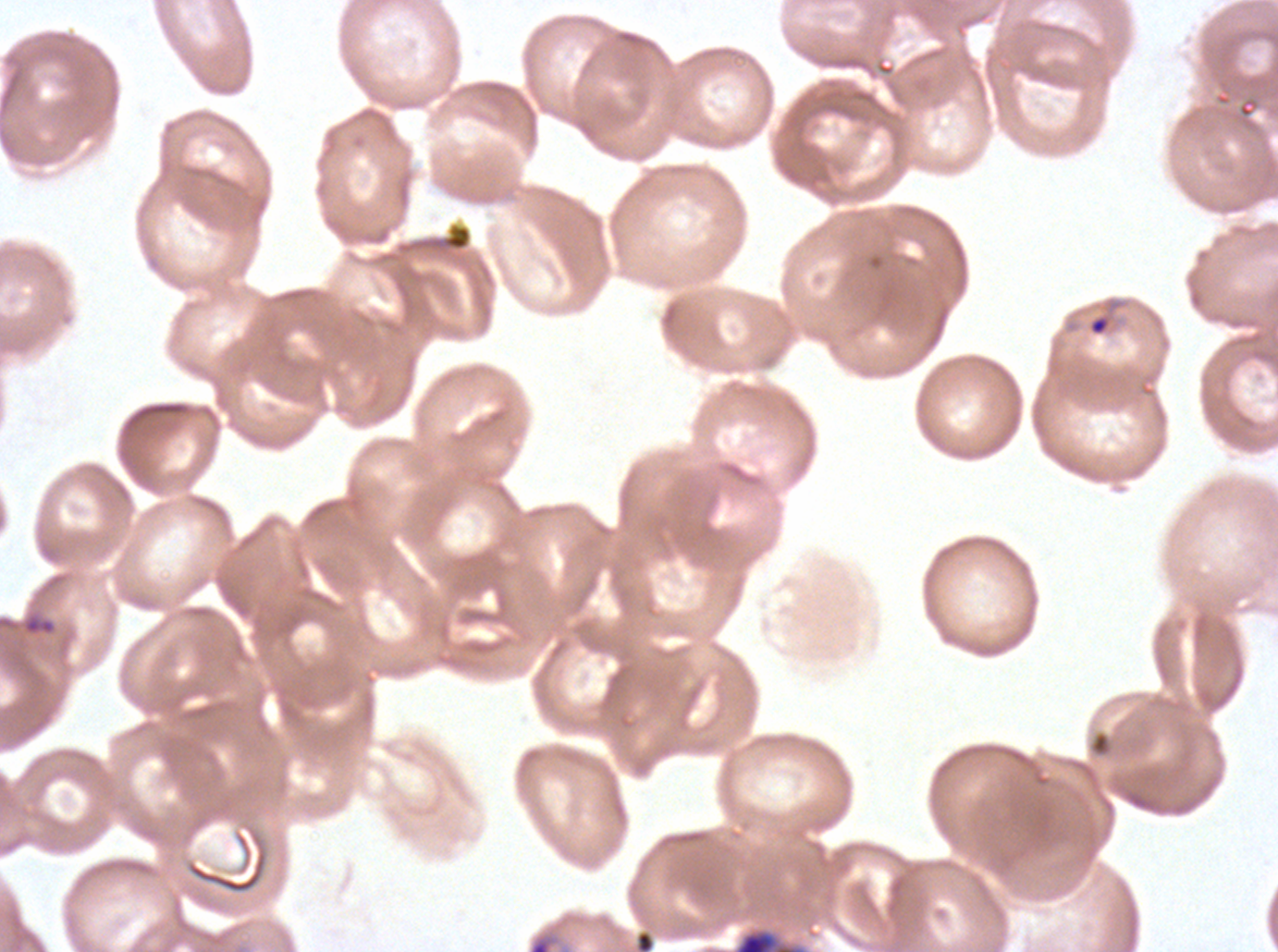
image_size: 1278×952 pixels
preparation: thin blood smear
ring_locations: 'approximate bounding boxes as {x1, y1, x2, y2} in pixels: {1086, 297, 1126, 337}, {527, 927, 572, 951}'
field_of_view: sub-image separated from a larger composite
specimen: P. falciparum cultured ex vivo for 24 to 48 hours, from a patient in The Gambia
stain: Giemsa
debris_locations: 'approximate bounding boxes as {x1, y1, x2, y2} in pixels: {21, 612, 57, 637}, {733, 927, 805, 951}'